Report the malaria status of this cell.
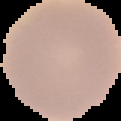
It is uninfected.

Cell region segmented out of the field of view; the surrounding area is masked to black. From a thin blood film. Image is 121×121 pixels.